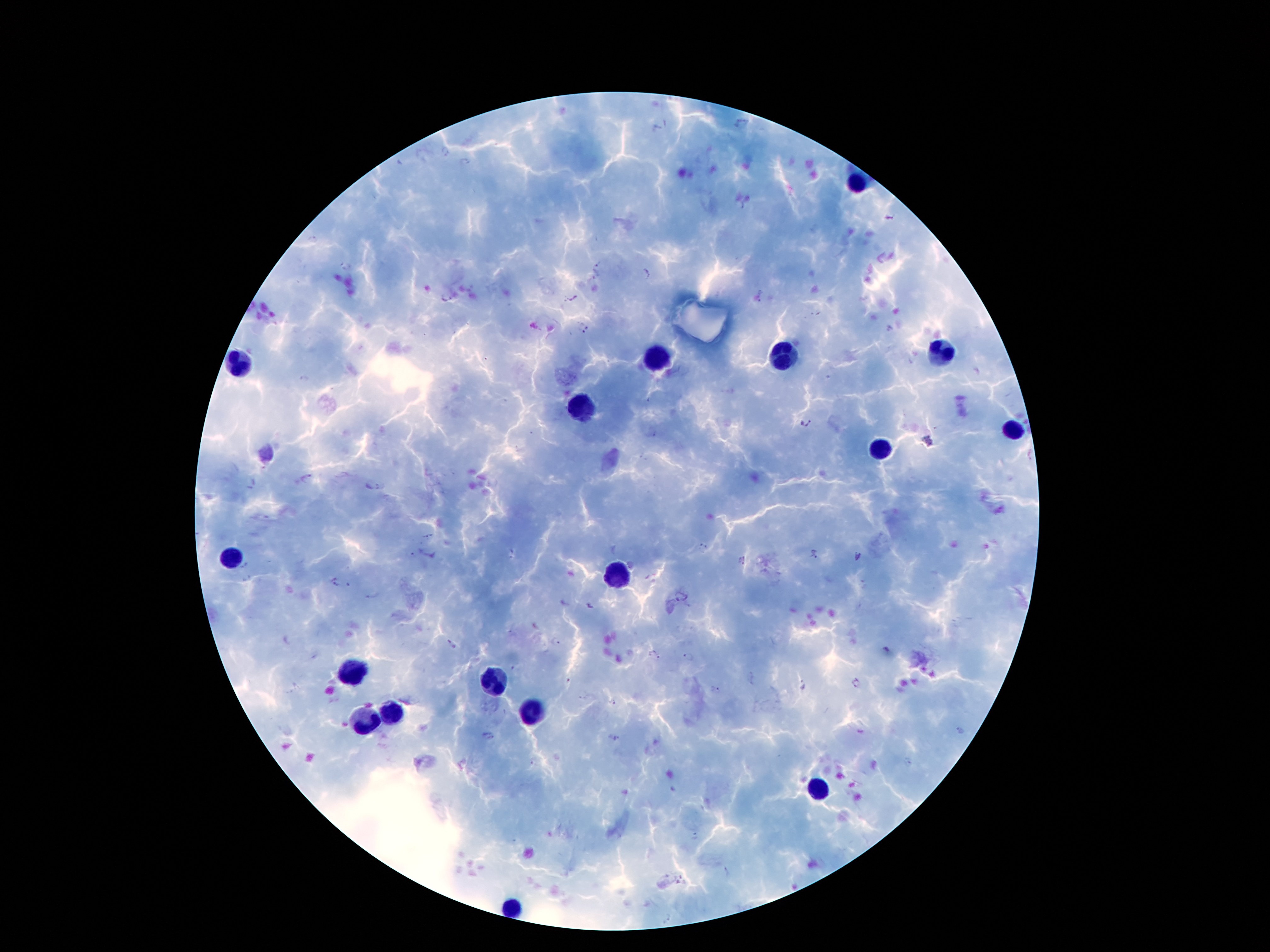
coordinate format = approximate centers as [x, y] in pixels
leukocyte locations = [857, 184], [939, 352], [783, 353], [658, 355], [241, 367], [579, 409], [1015, 431], [879, 449], [228, 559], [618, 577], [350, 672], [495, 683], [393, 713], [533, 713], [365, 723], [818, 792], [513, 907]
Plasmodium parasite locations = [444, 153], [465, 165], [888, 219], [312, 239], [599, 265], [345, 266], [648, 275], [444, 298], [584, 328], [304, 381], [807, 424], [929, 441], [428, 537], [702, 546], [815, 556], [741, 562], [246, 566], [337, 583], [372, 596], [556, 642], [451, 644], [654, 656], [688, 657], [569, 681], [855, 683], [803, 686], [715, 691], [613, 702], [960, 730], [613, 737], [692, 836], [728, 873], [668, 919]
image size = 1270×952 pixels
preparation = thick blood film
stain = Giemsa
capture = smartphone camera through the microscope eyepiece
magnification = 100x
patient malaria status = positive for Plasmodium falciparum
field of view = single